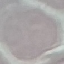
Summary:
  - Malaria status: uninfected
  - Preparation: thin blood smear
  - Stain: Giemsa
  - Capture: smartphone camera at the microscope eyepiece
  - Image type: cell patch, automatically extracted from a larger field of view and resized to 64 × 64 pixels